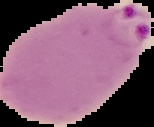
Summary:
  - Image size: 154×127 pixels
  - Result: Plasmodium parasites detected
  - Image type: segmented cell region with the area outside set to black
  - Preparation: thin blood film